Assess this cell for malaria.
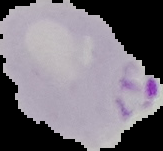
Parasitized.

Summary:
  - Image type: segmented cell region on a black background
  - Preparation: thin blood smear
  - Image size: 163×151 pixels